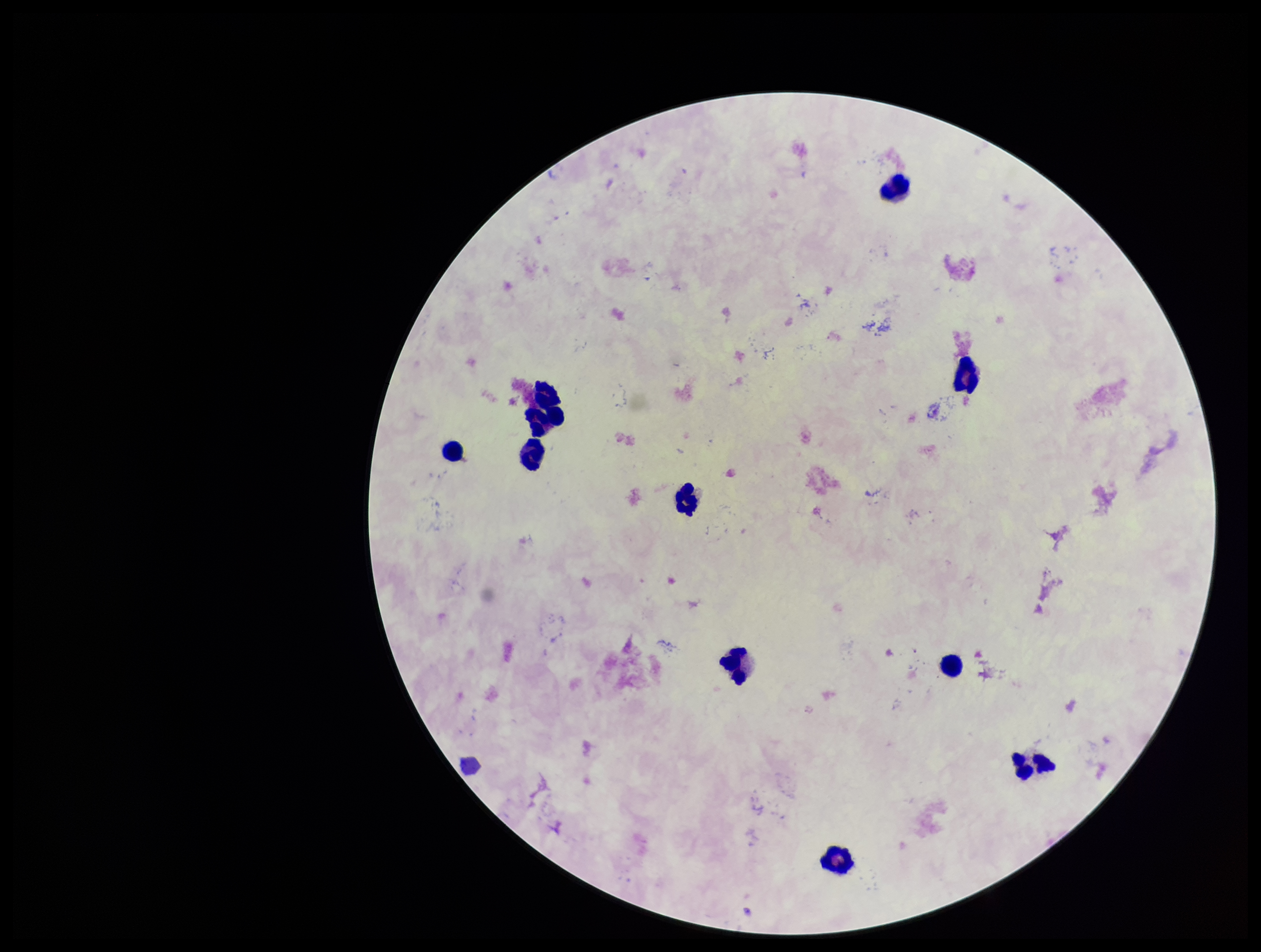
Summary:
  - Preparation: thick
  - Stain: Giemsa
  - Image size: 1261×952 pixels
  - Leukocyte count: 11
  - Field of view: single
  - Patient malaria status: negative
  - Plasmodium parasites: none identified
  - Parasite count: 0
  - Capture: smartphone photograph through the microscope eyepiece